Name the blood parasite species.
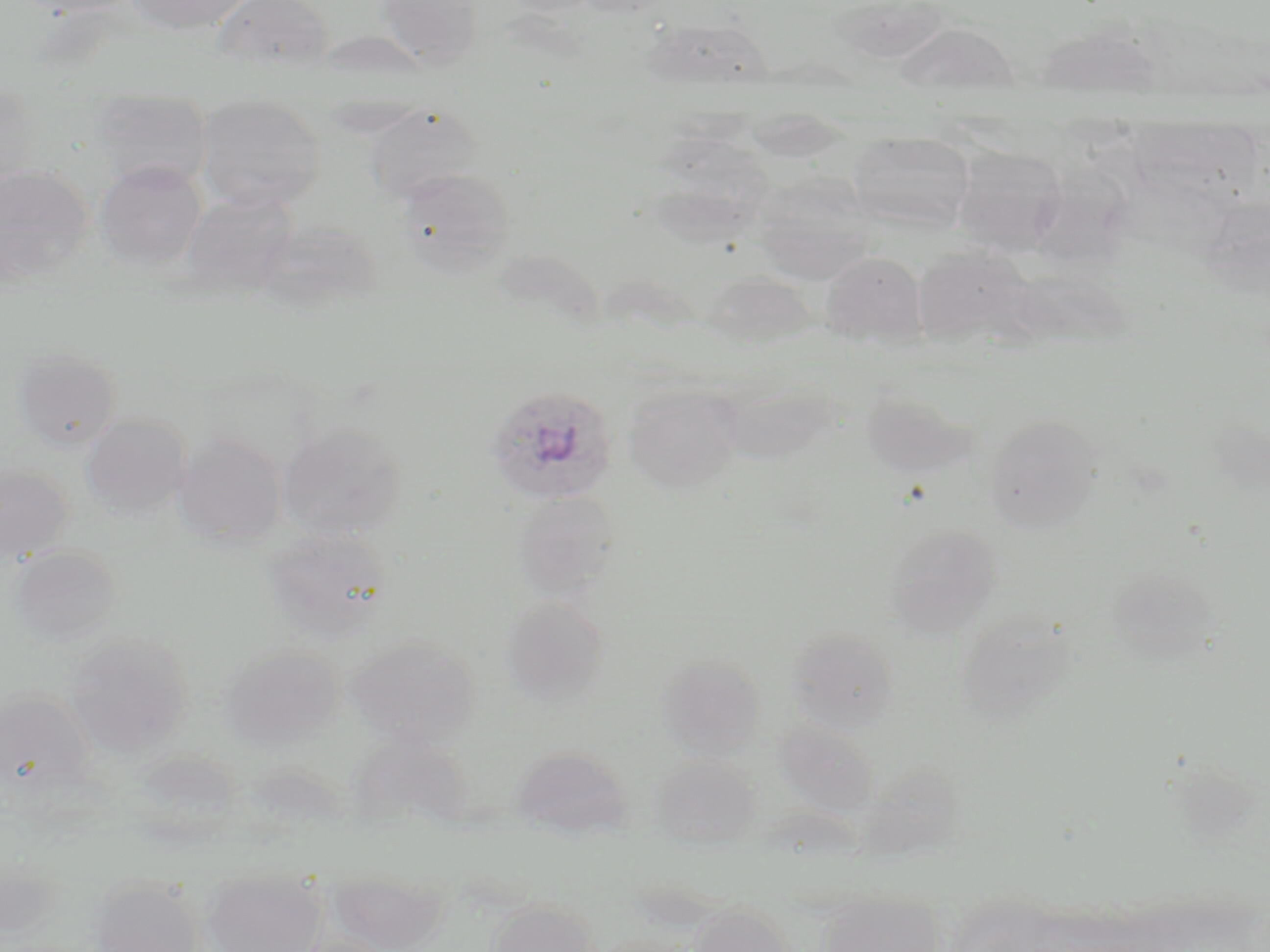
Plasmodium ovale.

stain = May-Grünwald-Giemsa
preparation = thin blood smear
uninfected red blood cell locations = approximate bounding boxes as named x1/y1/x2/y2 corners in pixels: (x1=125, y1=0, x2=255, y2=35), (x1=212, y1=0, x2=335, y2=74), (x1=376, y1=0, x2=484, y2=71), (x1=501, y1=0, x2=603, y2=18), (x1=894, y1=22, x2=1019, y2=101), (x1=0, y1=90, x2=40, y2=191), (x1=196, y1=93, x2=325, y2=212), (x1=92, y1=96, x2=212, y2=191), (x1=365, y1=103, x2=482, y2=204), (x1=1131, y1=111, x2=1256, y2=215), (x1=847, y1=132, x2=975, y2=232), (x1=952, y1=145, x2=1068, y2=254), (x1=95, y1=161, x2=206, y2=271), (x1=0, y1=164, x2=93, y2=287), (x1=397, y1=167, x2=516, y2=276), (x1=762, y1=172, x2=885, y2=283), (x1=179, y1=189, x2=299, y2=300), (x1=257, y1=218, x2=383, y2=313), (x1=913, y1=245, x2=1034, y2=349), (x1=821, y1=252, x2=926, y2=347), (x1=700, y1=271, x2=815, y2=349), (x1=13, y1=347, x2=121, y2=452), (x1=719, y1=373, x2=839, y2=464), (x1=623, y1=383, x2=742, y2=496), (x1=860, y1=386, x2=973, y2=479), (x1=81, y1=413, x2=190, y2=517), (x1=985, y1=413, x2=1102, y2=533), (x1=277, y1=422, x2=408, y2=541), (x1=173, y1=434, x2=286, y2=546), (x1=0, y1=464, x2=72, y2=564), (x1=511, y1=491, x2=620, y2=600), (x1=885, y1=523, x2=1002, y2=636), (x1=265, y1=526, x2=392, y2=642), (x1=9, y1=545, x2=120, y2=647), (x1=500, y1=595, x2=610, y2=709), (x1=954, y1=611, x2=1077, y2=723), (x1=786, y1=627, x2=899, y2=733), (x1=65, y1=634, x2=192, y2=755), (x1=347, y1=636, x2=478, y2=747), (x1=222, y1=645, x2=344, y2=747), (x1=657, y1=655, x2=766, y2=759), (x1=0, y1=690, x2=93, y2=799), (x1=775, y1=721, x2=879, y2=816), (x1=512, y1=745, x2=632, y2=839), (x1=126, y1=751, x2=243, y2=848), (x1=651, y1=752, x2=760, y2=849), (x1=1, y1=859, x2=61, y2=942), (x1=326, y1=869, x2=449, y2=951), (x1=201, y1=870, x2=325, y2=952), (x1=88, y1=876, x2=204, y2=952), (x1=819, y1=889, x2=946, y2=952), (x1=488, y1=900, x2=599, y2=952), (x1=688, y1=903, x2=795, y2=952), (x1=593, y1=933, x2=695, y2=952)
magnification = 1000x
image size = 1270×952 pixels
field of view = single
modality = light microscopy
Plasmodium ovale-infected red blood cell locations = approximate bounding boxes as named x1/y1/x2/y2 corners in pixels: (x1=484, y1=383, x2=619, y2=507)